State which parasite is depicted.
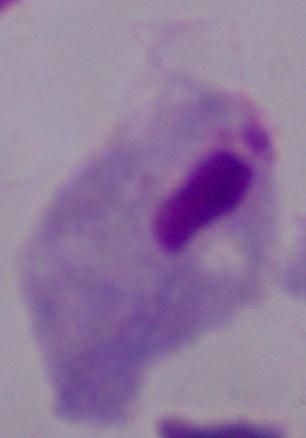
This is a trichomonad.

Summary:
  - Magnification: 1000x
  - Modality: micrograph